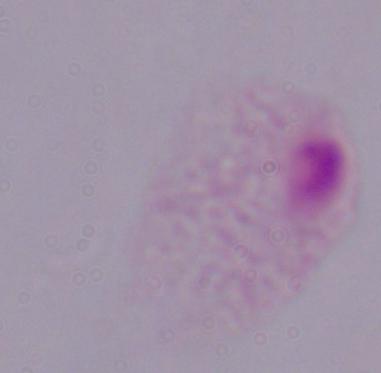

Summary:
  - Identification: trichomonad
  - Modality: micrograph
  - Magnification: 1000x